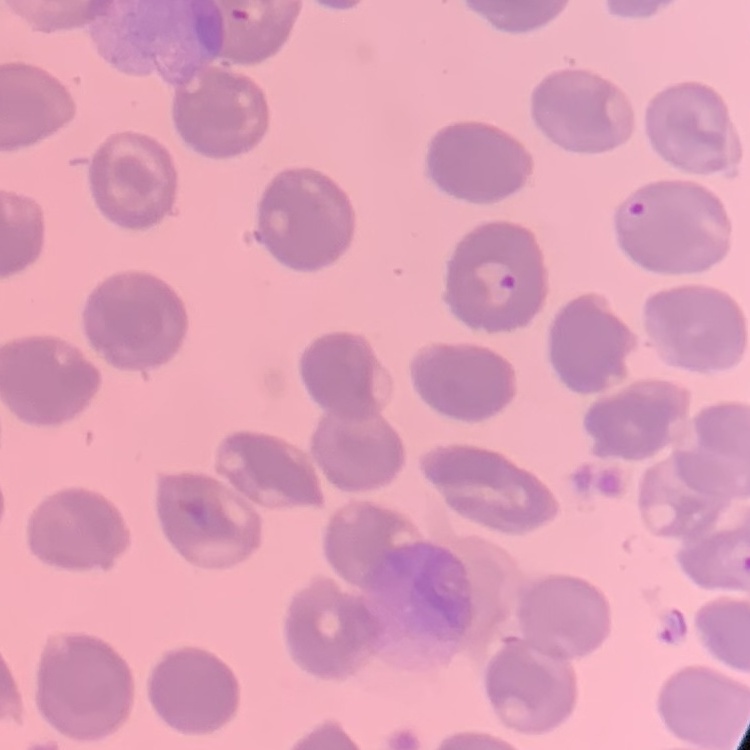

erythrocyte morphology = no rouleaux formation
image type = square crop of a larger photomicrograph
preparation = thin peripheral smear
stain = Field's or Giemsa